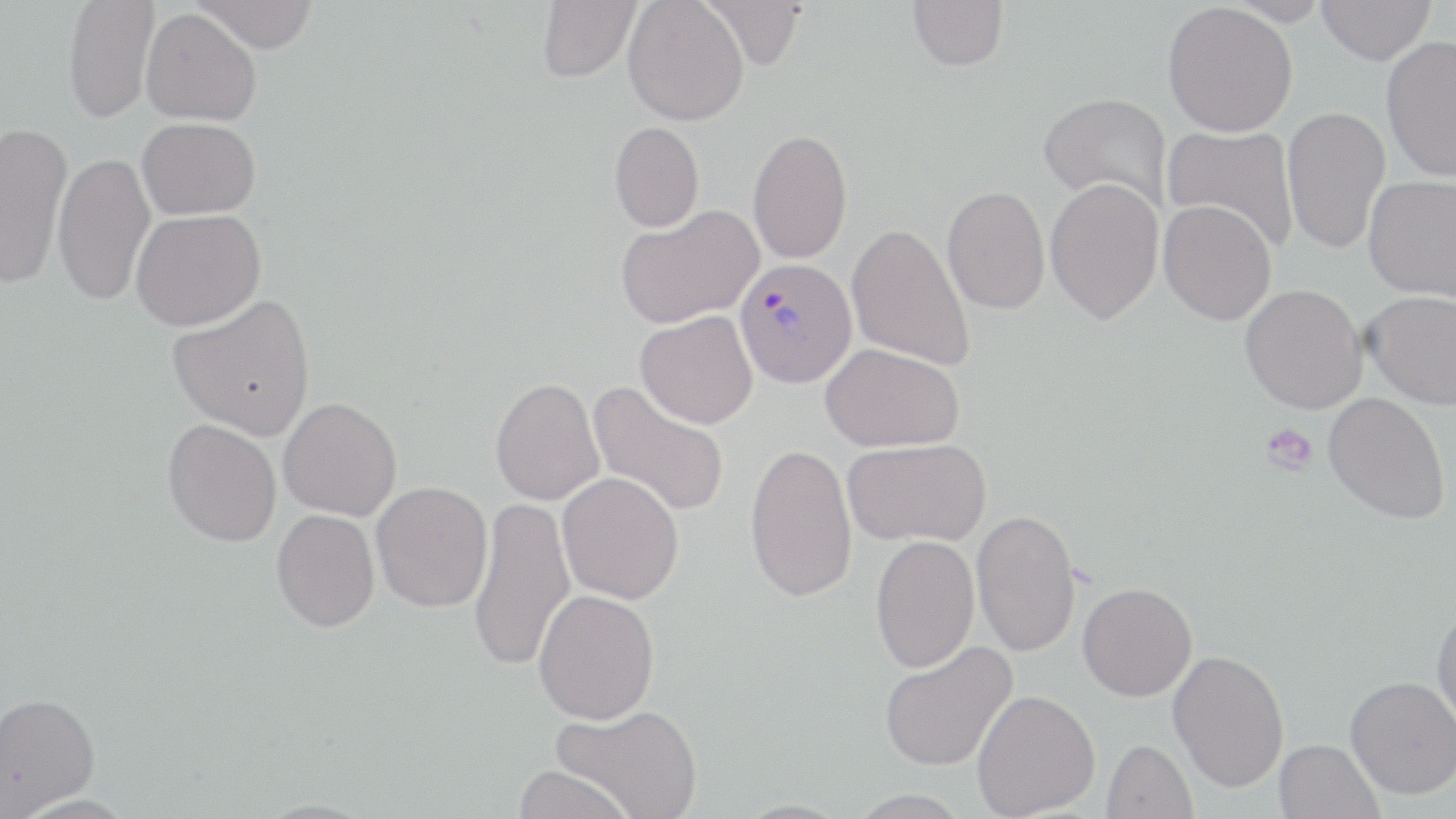

slide-level diagnosis = Plasmodium vivax
magnification = 1000x
field of view = single
platelet locations = approximate bounding boxes as named x1/y1/x2/y2 corners in pixels: (x1=1261, y1=424, x2=1318, y2=476)
image size = 1456×819 pixels
Plasmodium vivax-infected red blood cell locations = approximate bounding boxes as named x1/y1/x2/y2 corners in pixels: (x1=734, y1=258, x2=857, y2=388)
preparation = thin blood film
stain = May-Grünwald-Giemsa
uninfected red blood cell locations = approximate bounding boxes as named x1/y1/x2/y2 corners in pixels: (x1=63, y1=0, x2=159, y2=123), (x1=190, y1=0, x2=319, y2=54), (x1=536, y1=0, x2=641, y2=82), (x1=623, y1=0, x2=748, y2=126), (x1=699, y1=0, x2=808, y2=70), (x1=1223, y1=0, x2=1332, y2=26), (x1=1317, y1=0, x2=1435, y2=65), (x1=907, y1=1, x2=1008, y2=71), (x1=1162, y1=2, x2=1298, y2=137), (x1=141, y1=8, x2=261, y2=126), (x1=1381, y1=35, x2=1456, y2=182), (x1=1039, y1=92, x2=1172, y2=212), (x1=1282, y1=106, x2=1391, y2=255), (x1=137, y1=117, x2=261, y2=219), (x1=0, y1=121, x2=71, y2=290), (x1=608, y1=122, x2=704, y2=232), (x1=1162, y1=125, x2=1299, y2=254), (x1=748, y1=128, x2=852, y2=264), (x1=52, y1=152, x2=156, y2=306), (x1=1363, y1=175, x2=1456, y2=302), (x1=1045, y1=178, x2=1164, y2=325), (x1=941, y1=186, x2=1050, y2=315), (x1=1158, y1=200, x2=1277, y2=325), (x1=616, y1=205, x2=764, y2=329), (x1=130, y1=209, x2=266, y2=331), (x1=847, y1=223, x2=976, y2=372), (x1=1240, y1=283, x2=1368, y2=413), (x1=1362, y1=290, x2=1456, y2=410), (x1=167, y1=294, x2=316, y2=440), (x1=635, y1=310, x2=758, y2=429), (x1=821, y1=343, x2=965, y2=452), (x1=490, y1=376, x2=605, y2=506), (x1=587, y1=380, x2=730, y2=519), (x1=1324, y1=392, x2=1451, y2=525), (x1=278, y1=397, x2=401, y2=520), (x1=163, y1=419, x2=282, y2=547), (x1=842, y1=437, x2=991, y2=547), (x1=745, y1=443, x2=858, y2=604), (x1=557, y1=472, x2=684, y2=604), (x1=371, y1=481, x2=493, y2=612), (x1=468, y1=495, x2=575, y2=674), (x1=971, y1=508, x2=1081, y2=658), (x1=271, y1=509, x2=380, y2=632), (x1=870, y1=535, x2=980, y2=673), (x1=1078, y1=581, x2=1198, y2=701), (x1=533, y1=589, x2=660, y2=724), (x1=1431, y1=604, x2=1456, y2=735), (x1=879, y1=640, x2=1017, y2=771), (x1=1168, y1=648, x2=1290, y2=794), (x1=1345, y1=676, x2=1456, y2=799), (x1=971, y1=689, x2=1100, y2=818), (x1=0, y1=691, x2=101, y2=816), (x1=550, y1=704, x2=704, y2=818), (x1=1101, y1=739, x2=1197, y2=819), (x1=1274, y1=739, x2=1384, y2=819), (x1=511, y1=765, x2=636, y2=818), (x1=847, y1=788, x2=972, y2=818)
modality = light microscopy